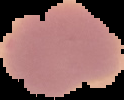
preparation = thin blood smear
image type = segmented cell region with the area outside set to black
malaria status = uninfected
image size = 124×100 pixels